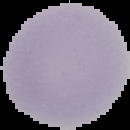

Image is 130×130 pixels. The area outside the segmented cell region is set to black. Malaria status: uninfected. From a thin blood film.